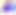
{
  "modality": "photomicrograph",
  "identification": "Toxoplasma gondii",
  "magnification": "400x"
}